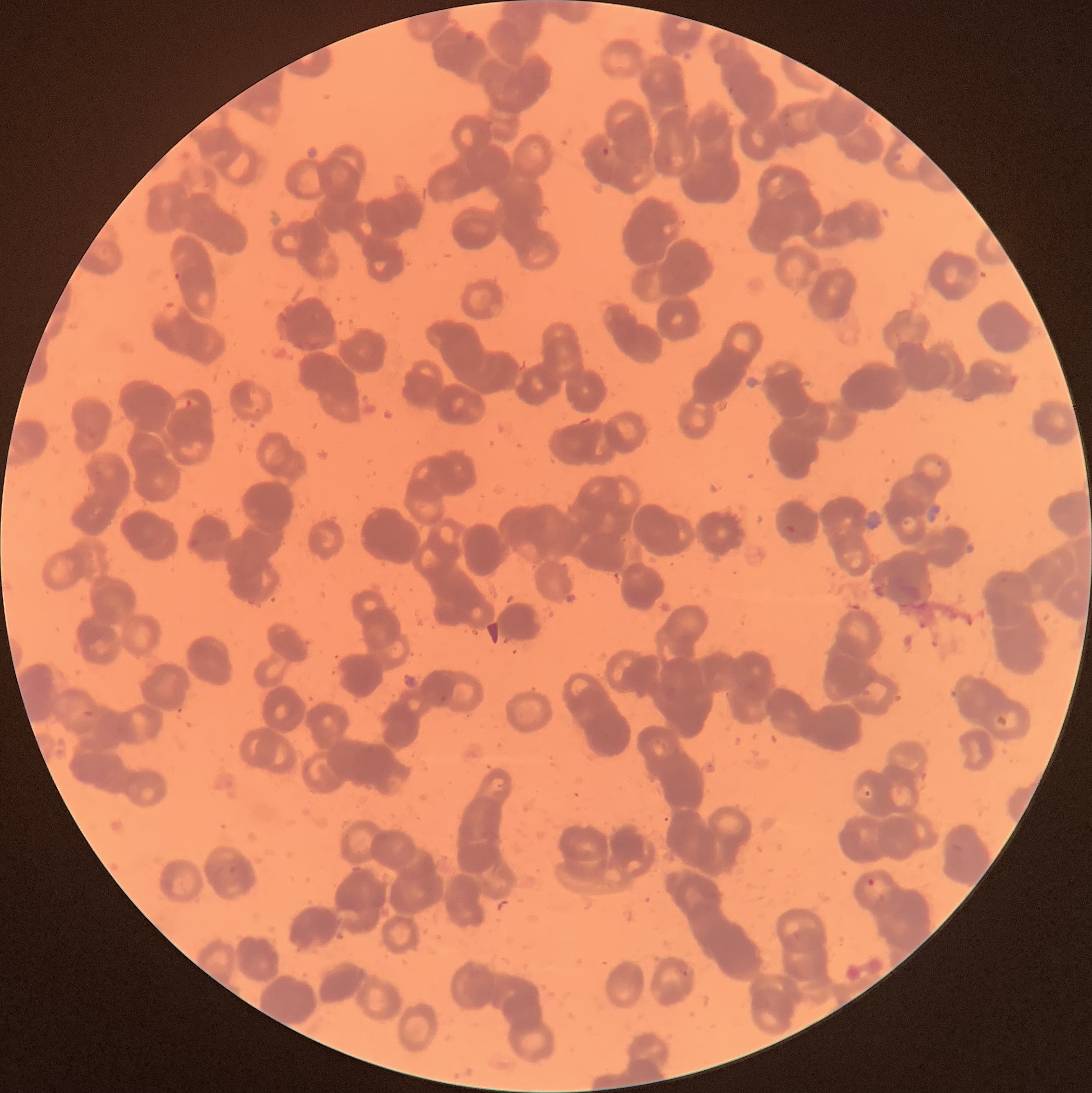
Approximate bounding boxes as [x1, y1, x2, y2] in pixels. Plasmodium parasite locations: [600, 146, 612, 158], [174, 270, 183, 282], [183, 397, 195, 410], [786, 523, 798, 535], [863, 789, 871, 798], [864, 876, 875, 888]. Light microscopy. Image is 1092×1093 pixels. Thin blood smear. The red blood cells show rouleaux formation.